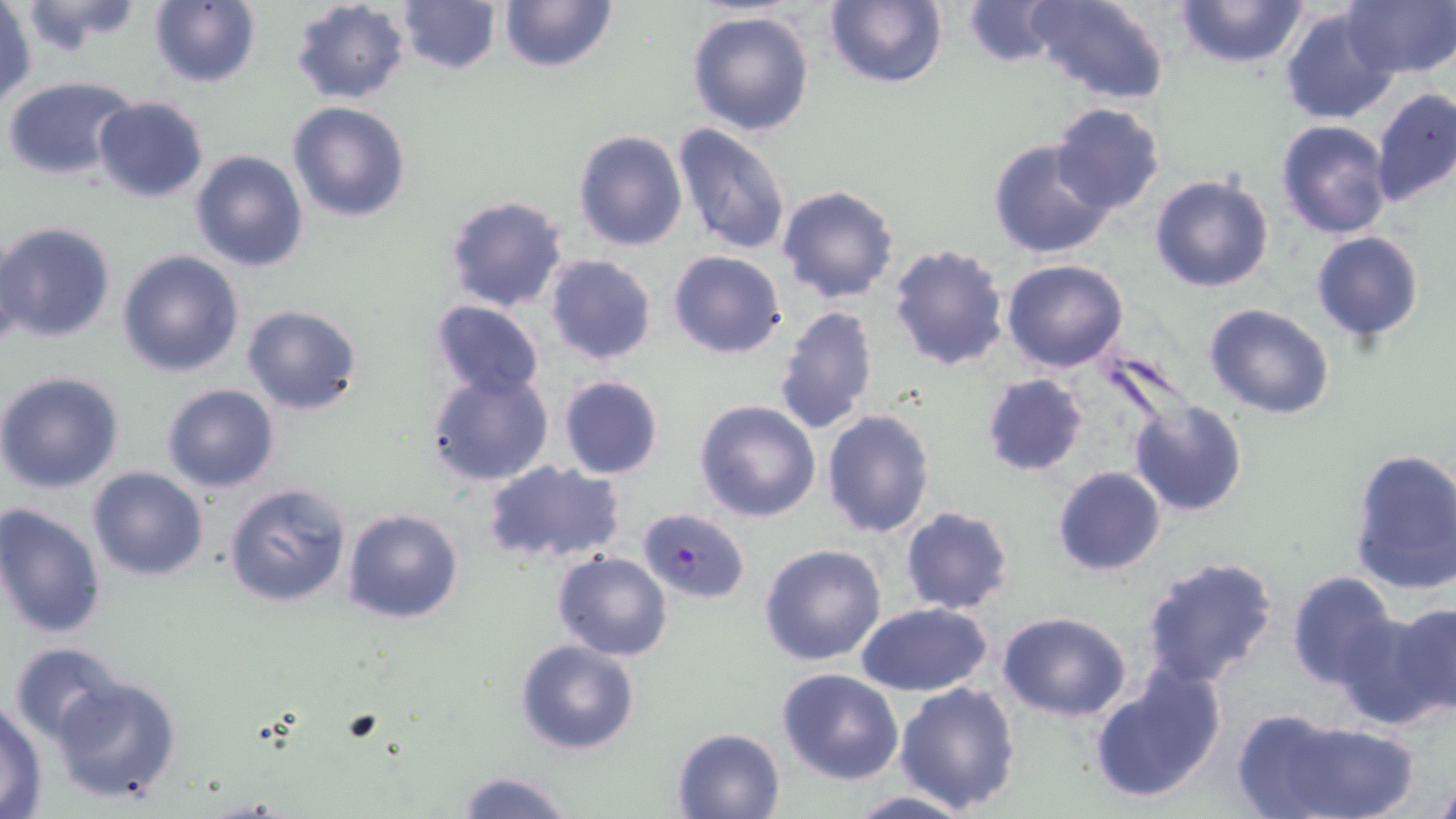

Summary:
  - Coordinate format: approximate bounding boxes as (x1, y1, x2, y2) in pixels
  - Uninfected red blood cell locations: (17, 0, 145, 53), (147, 0, 261, 88), (288, 0, 410, 104), (496, 0, 618, 73), (824, 0, 948, 89), (1029, 0, 1172, 106), (1173, 0, 1312, 70), (1341, 0, 1455, 79), (396, 1, 501, 76), (957, 1, 1073, 69), (1280, 4, 1403, 123), (1, 6, 36, 106), (687, 8, 817, 137), (3, 77, 141, 183), (1370, 87, 1456, 208), (93, 96, 210, 202), (287, 100, 413, 223), (1050, 101, 1166, 214), (1277, 119, 1393, 238), (671, 121, 793, 256), (572, 129, 689, 252), (988, 138, 1116, 259), (190, 150, 309, 274), (1149, 172, 1276, 294), (776, 184, 900, 304), (442, 195, 569, 314), (0, 220, 116, 343), (1310, 231, 1426, 342), (887, 242, 1011, 372), (116, 249, 243, 378), (667, 250, 787, 359), (543, 255, 658, 366), (1002, 258, 1128, 371), (429, 300, 545, 400), (241, 304, 364, 416), (774, 304, 878, 435), (1204, 304, 1335, 419), (426, 368, 555, 488), (0, 371, 126, 494), (979, 372, 1090, 476), (557, 374, 665, 480), (160, 384, 280, 494), (694, 399, 822, 521), (1130, 401, 1248, 516), (821, 408, 936, 538), (1347, 446, 1456, 596), (482, 459, 625, 566), (1052, 466, 1166, 577), (86, 467, 210, 581), (223, 481, 352, 609), (0, 502, 108, 639), (899, 506, 1016, 616), (342, 508, 464, 625), (758, 543, 887, 667), (552, 550, 673, 660), (533, 552, 658, 753), (1139, 556, 1279, 688), (1285, 572, 1399, 691), (856, 603, 993, 697), (1391, 605, 1456, 712), (1333, 607, 1455, 730), (998, 612, 1132, 722), (515, 638, 639, 755), (9, 641, 126, 746), (1086, 667, 1225, 805), (777, 668, 904, 785), (48, 672, 182, 804), (894, 681, 1021, 813), (0, 698, 48, 817), (1256, 717, 1417, 819), (671, 727, 785, 818), (1429, 763, 1456, 819), (455, 770, 574, 819), (842, 791, 975, 819)
  - Plasmodium falciparum-infected red blood cell locations: (636, 508, 749, 605)
  - Slide-level diagnosis: Plasmodium falciparum
  - Magnification: 1000x
  - Field of view: single
  - Preparation: thin blood smear
  - Modality: optical microscopy
  - Image size: 1456×819 pixels
  - Stain: May-Grünwald-Giemsa